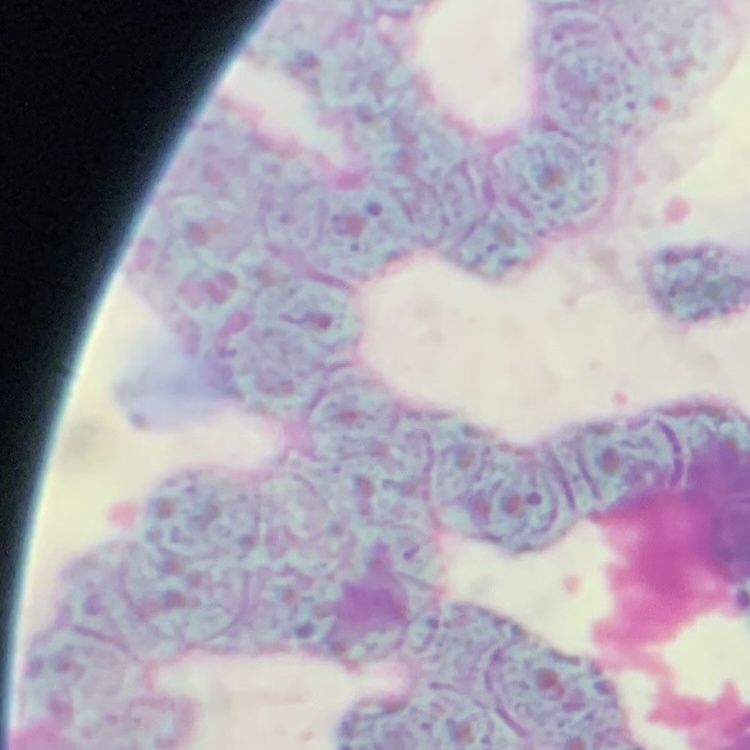

Summary:
  - Red blood cell morphology: rouleaux formation
  - Stain: Field's or Giemsa
  - Preparation: thin peripheral smear
  - Image type: square crop of a larger photomicrograph